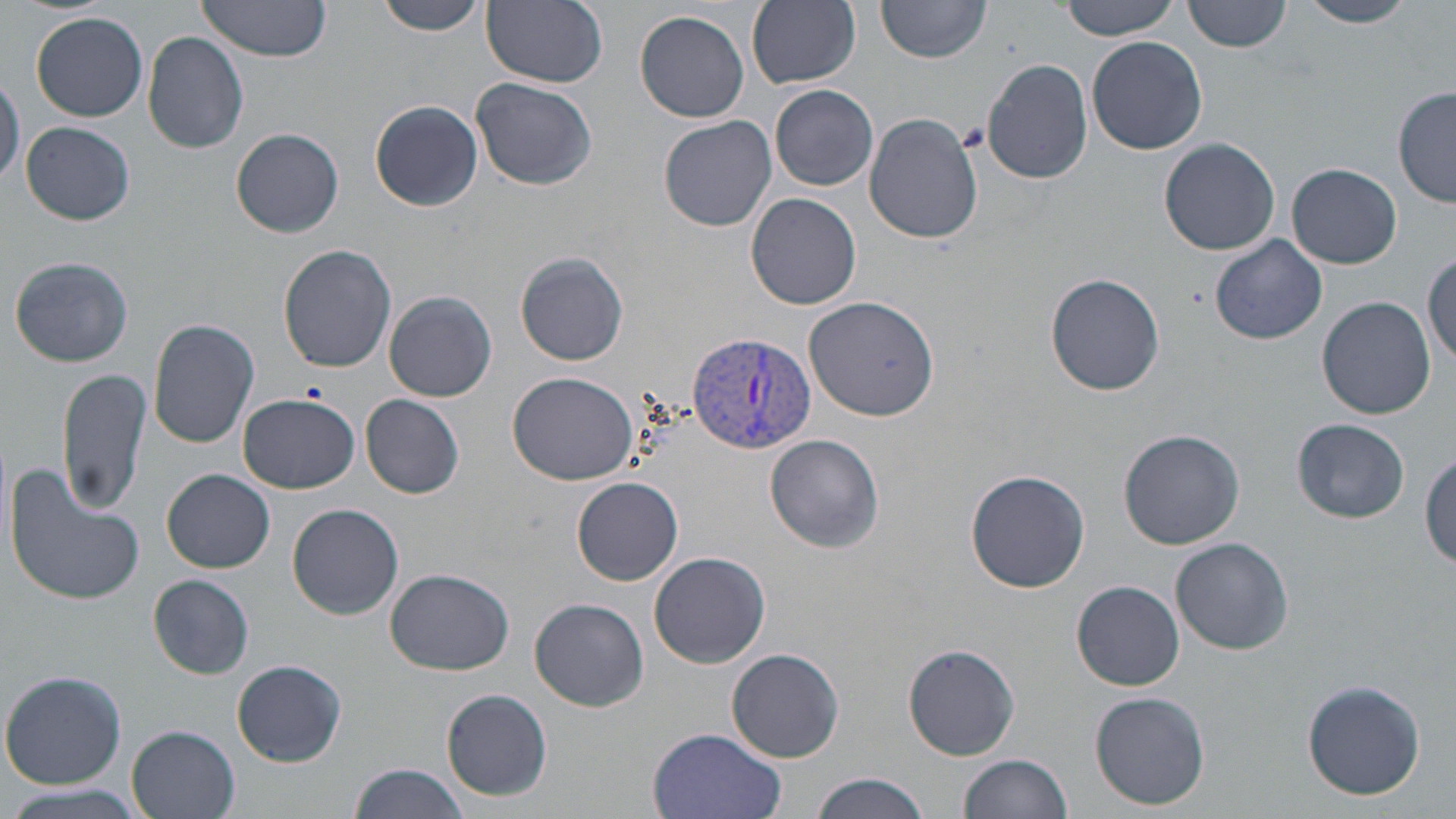
Approximate bounding boxes as (x1, y1, x2, y2) in pixels. Uninfected red blood cell locations: (192, 0, 336, 67), (376, 0, 487, 35), (1059, 0, 1182, 39), (1185, 0, 1291, 53), (1297, 0, 1419, 27), (480, 1, 608, 89), (747, 1, 860, 88), (877, 2, 992, 66), (636, 10, 750, 123), (31, 12, 148, 122), (143, 30, 249, 154), (1087, 35, 1207, 155), (982, 57, 1093, 183), (0, 74, 23, 190), (471, 76, 597, 191), (770, 83, 879, 191), (1395, 88, 1455, 209), (371, 101, 482, 212), (863, 112, 984, 245), (659, 115, 777, 232), (20, 121, 135, 225), (231, 128, 344, 238), (1159, 138, 1282, 255), (1288, 162, 1401, 270), (746, 192, 862, 310), (1210, 234, 1327, 346), (278, 244, 397, 373), (516, 252, 628, 366), (1425, 252, 1456, 366), (9, 256, 134, 367), (1041, 273, 1161, 395), (384, 291, 497, 401), (805, 296, 939, 420), (1317, 297, 1436, 420), (148, 318, 260, 449), (57, 368, 151, 517), (508, 372, 640, 485), (237, 393, 360, 494), (361, 394, 464, 498), (1292, 418, 1410, 524), (1117, 429, 1244, 550), (767, 435, 883, 549), (1423, 450, 1456, 568), (5, 460, 147, 609), (966, 469, 1091, 593), (162, 470, 275, 574), (572, 477, 684, 585), (287, 503, 406, 619), (1171, 537, 1294, 654), (649, 551, 770, 668), (384, 568, 514, 676), (149, 576, 254, 679), (1071, 579, 1185, 691), (531, 597, 648, 712), (904, 644, 1020, 759), (728, 647, 845, 763), (233, 659, 347, 767), (1, 670, 126, 789), (1303, 678, 1427, 801), (442, 689, 551, 802), (1090, 690, 1211, 810), (127, 726, 240, 819), (647, 728, 787, 819), (958, 754, 1074, 819), (350, 762, 472, 819), (810, 773, 934, 819), (0, 780, 151, 819). Platelet locations: (955, 122, 989, 153), (301, 379, 329, 403). Plasmodium vivax-infected red blood cell locations: (689, 333, 819, 455). Slide-level diagnosis: Plasmodium vivax. Thin blood film. May-Grünwald-Giemsa-stained preparation. 1000x magnification. One field of a larger specimen. Image is 1456×819 pixels. Light microscopy.